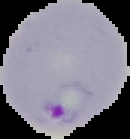

Summary:
  - Image type: segmented cell region on a black background
  - Preparation: thin blood film
  - Result: malaria parasites identified
  - Image size: 130×139 pixels